Comment on the morphology of the red blood cells.
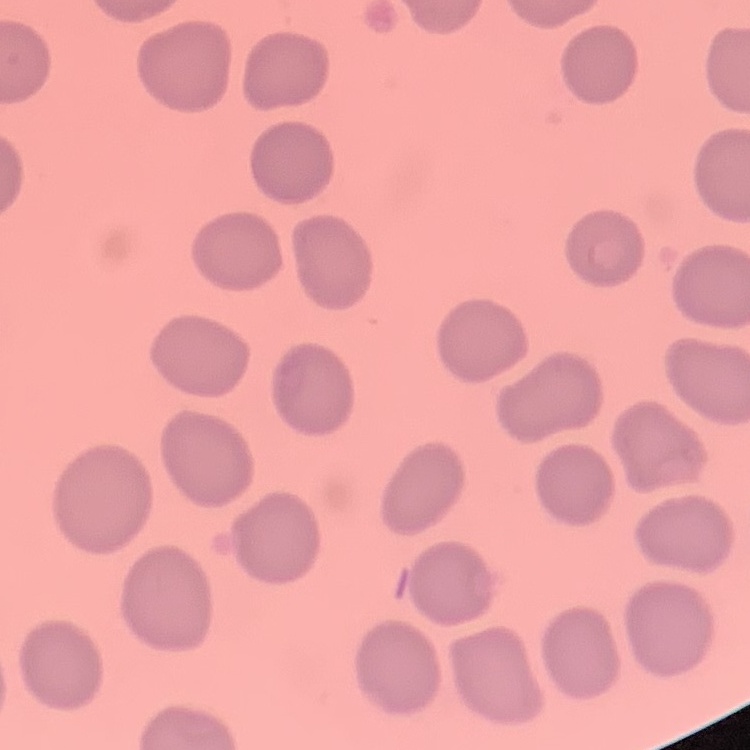

No rouleaux formation.

One tile cut from a larger photomicrograph. Stained with either Field's or Giemsa. Thin blood smear.